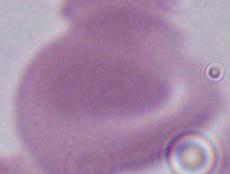
Summary:
  - Identification: red blood cell
  - Magnification: 1000x
  - Modality: photomicrograph